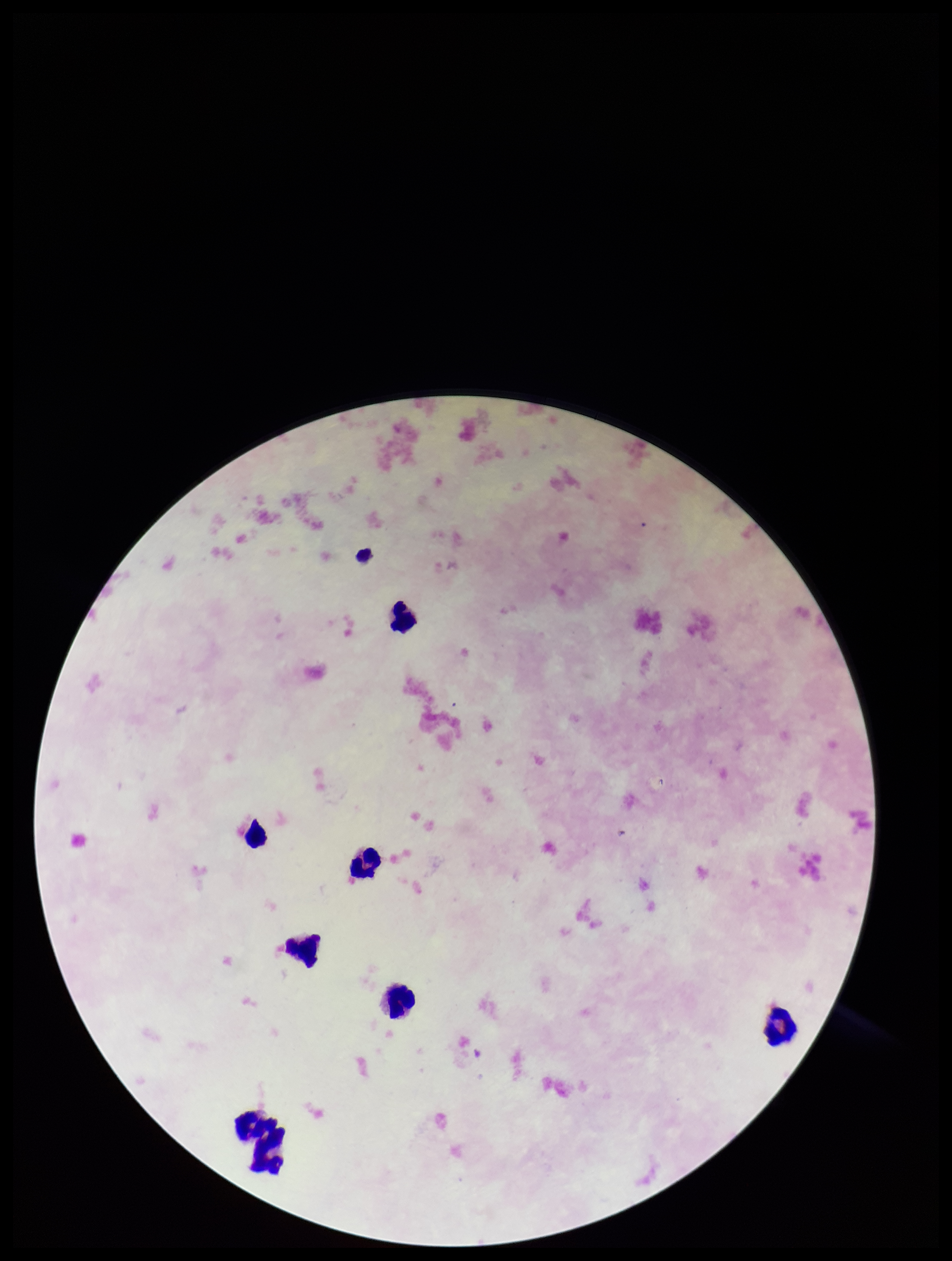

{
  "image_size": "952×1261 pixels",
  "leukocyte_count": 8,
  "preparation": "thick blood smear",
  "capture": "smartphone photograph through the microscope eyepiece",
  "field_of_view": "single",
  "patient_malaria_status": "negative",
  "stain": "Giemsa",
  "plasmodium_parasites": "none seen",
  "parasite_count": 0
}